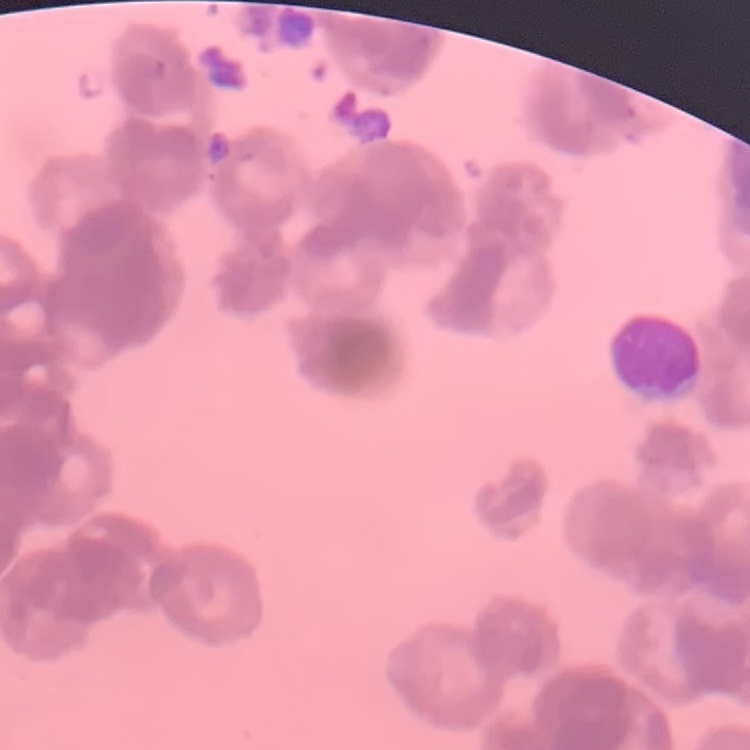

{
  "erythrocyte_morphology": "rouleaux formation",
  "stain": "Field's or Giemsa",
  "image_type": "square crop of a larger photomicrograph",
  "preparation": "thin blood smear"
}